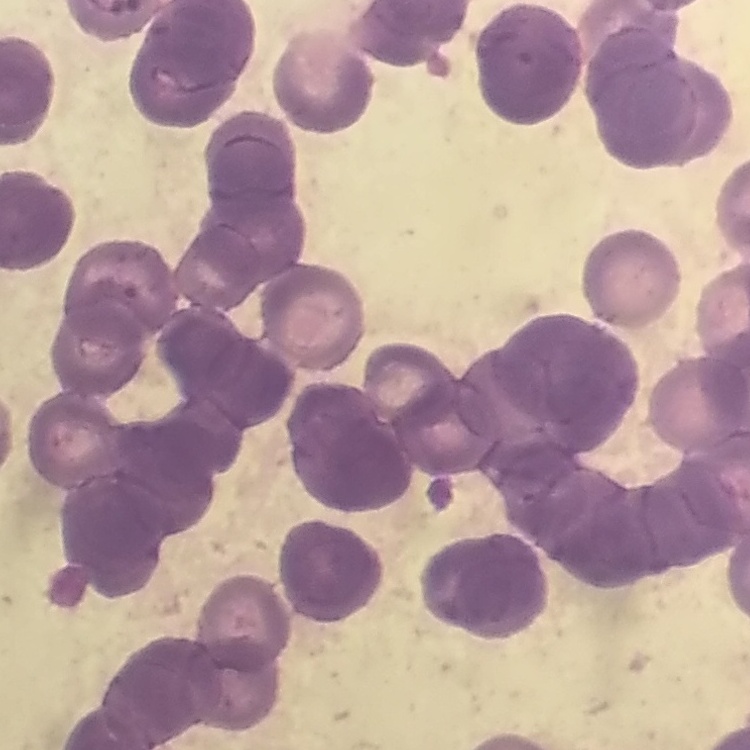

Summary:
  - Erythrocyte morphology: rouleaux formation
  - Image type: one tile cut from a larger photomicrograph
  - Preparation: thin blood smear
  - Stain: Field's or Giemsa